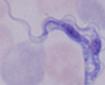

Summary:
  - Magnification: 1000x
  - Modality: micrograph
  - Identification: trypanosome